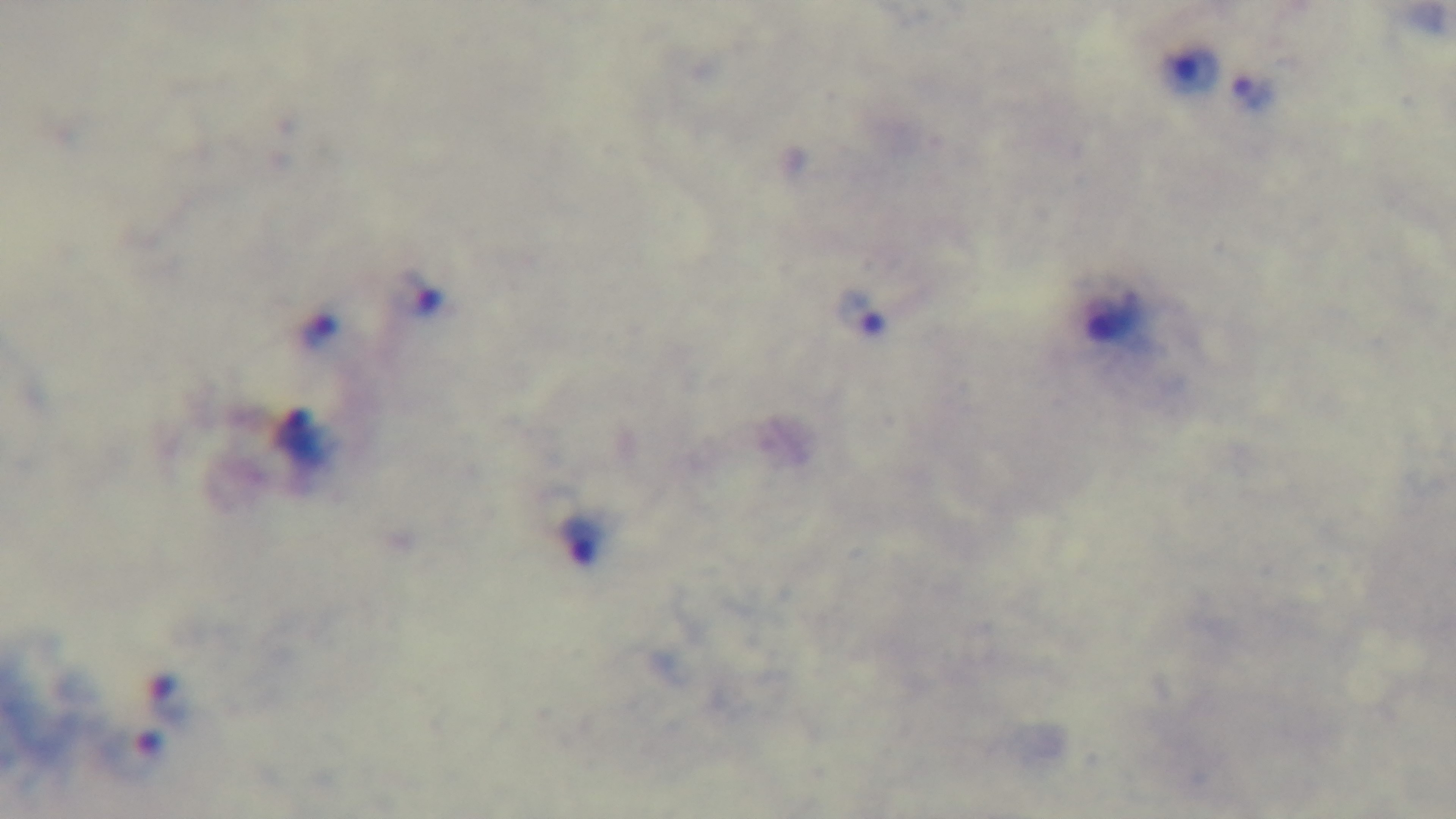
malaria status = infected
stain = Giemsa
modality = light microscopy
preparation = thick
capture = mounted 4K digital camera
field of view = one from the slide
objective = 100x oil immersion